Identify the parasite.
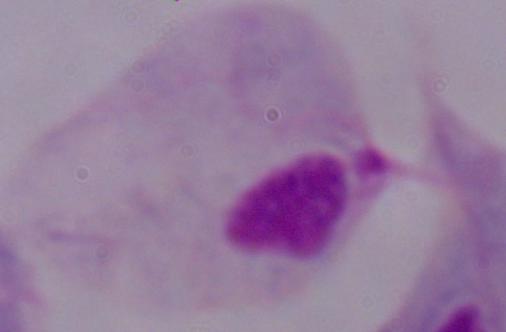

This is a trichomonad.

Summary:
  - Magnification: 1000x
  - Modality: photomicrograph